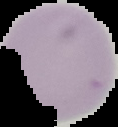

Summary:
  - Image size: 118×127 pixels
  - Image type: cell region segmented out of the field of view; surrounding area masked to black
  - Preparation: thin blood film
  - Result: negative for Plasmodium parasites